Name the cell type shown.
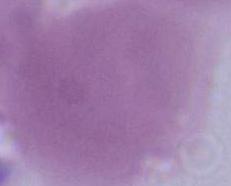
This is an erythrocyte.

Summary:
  - Modality: photomicrograph
  - Magnification: 1000x